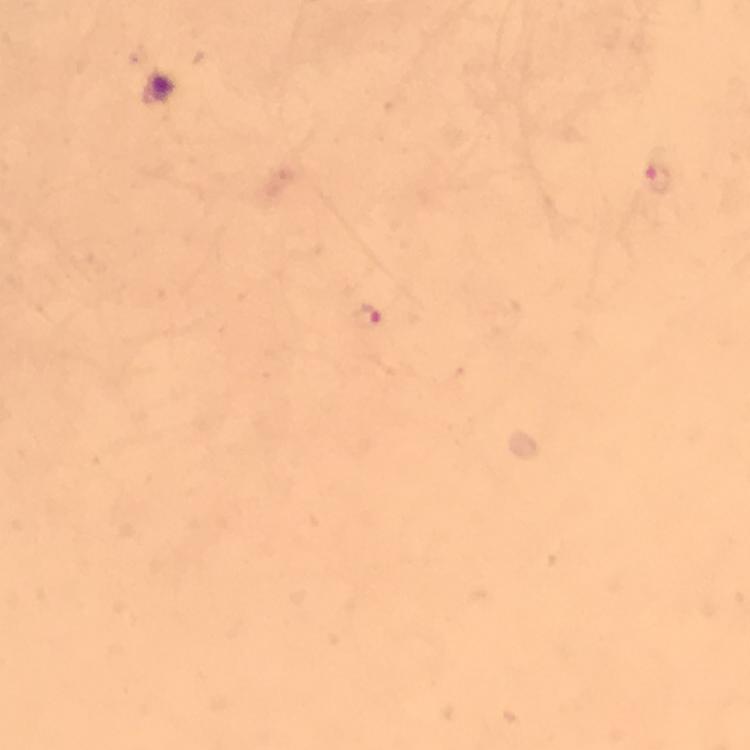

preparation = thick blood smear
malaria parasite locations = approximate centers as {x, y} in pixels: {655, 180}, {367, 318}
capture = smartphone photograph through a microscope
image size = 750×750 pixels
magnification = 100x
stain = Giemsa
cropped from = a single field of view
immersion oil = applied
context = from a malaria diagnostic workup